State which parasite is depicted.
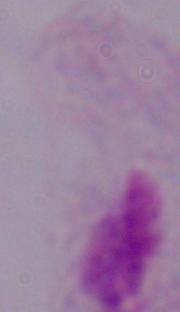

This is a trichomonad.

Summary:
  - Modality: photomicrograph
  - Magnification: 1000x